Identify the parasite.
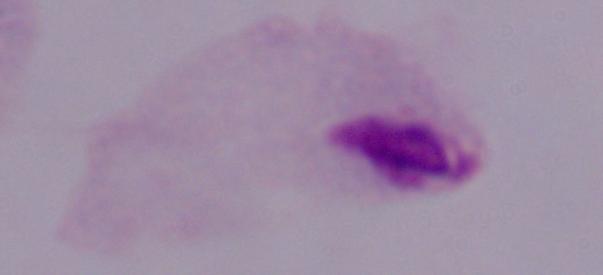

A trichomonad.

1000x magnification. Photomicrograph.